Assess this cell for malaria.
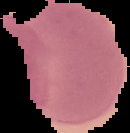

It is parasitized.

Summary:
  - Preparation: thin blood film
  - Image type: cell region segmented out of the field of view; surrounding area masked to black
  - Image size: 130×133 pixels